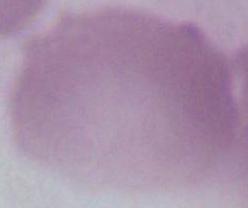 Captured at 1000x magnification. A red blood cell is seen. Photomicrograph.